Give the extent of all Plasmodium ovale-infected red blood cells.
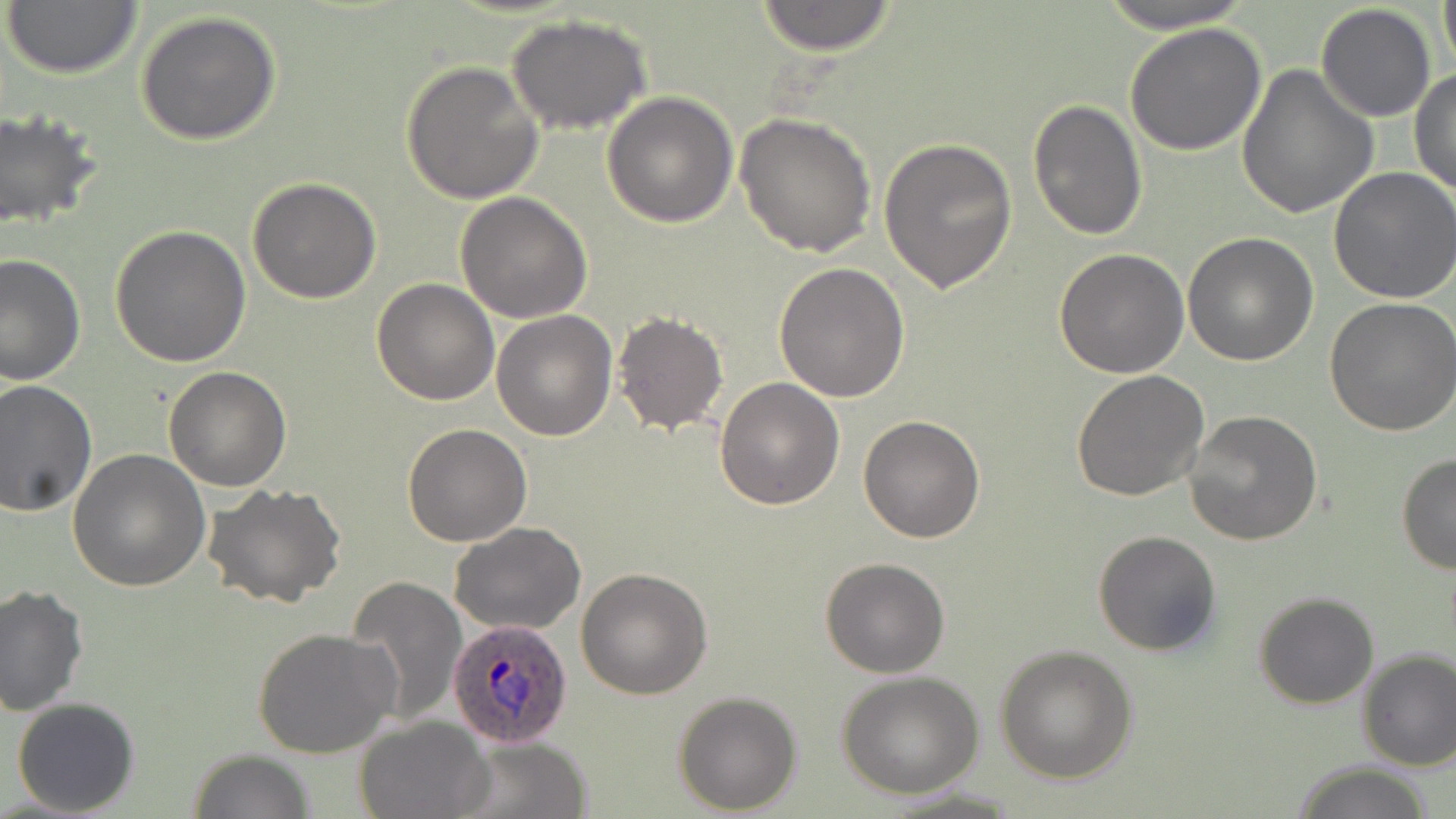

Approximate bounding boxes as (x1,y1)-(x2,y2) corner pairs in pixels.
Plasmodium ovale-infected red blood cells: (447,617)-(576,749).

Uninfected red blood cell locations: (752,0)-(900,54), (1091,0)-(1263,34), (1434,0)-(1456,75), (2,1)-(144,79), (1315,3)-(1437,121), (134,9)-(282,146), (506,15)-(655,135), (1124,22)-(1268,157), (400,60)-(544,205), (1238,65)-(1376,218), (1410,68)-(1455,197), (602,92)-(737,229), (1027,97)-(1148,240), (0,109)-(101,232), (732,112)-(878,256), (879,137)-(1020,295), (1328,167)-(1456,304), (247,176)-(382,303), (455,192)-(592,322), (110,225)-(251,367), (1182,231)-(1318,366), (1054,247)-(1189,377), (1,253)-(86,388), (773,261)-(910,402), (371,278)-(500,405), (1324,296)-(1456,436), (491,311)-(617,442), (612,311)-(729,437), (163,366)-(291,492), (1070,370)-(1209,503), (714,375)-(844,509), (0,380)-(97,516), (1184,409)-(1325,545), (857,414)-(986,542), (402,423)-(532,547), (67,449)-(210,593), (1395,453)-(1455,575), (203,483)-(348,607), (450,522)-(588,636), (1092,530)-(1221,657), (820,558)-(950,678), (575,567)-(713,699), (347,576)-(467,726), (0,584)-(90,719), (1253,592)-(1379,710), (253,627)-(399,760), (995,644)-(1138,783), (1356,648)-(1456,772), (835,670)-(985,798), (672,689)-(803,812), (11,696)-(141,817), (353,715)-(493,819), (452,736)-(594,819), (188,749)-(315,819), (1290,761)-(1438,819). Slide-level diagnosis: Plasmodium ovale. May-Grünwald-Giemsa-stained preparation. 1000x magnification. One field of a larger specimen. Thin blood film. Image is 1456×819 pixels. Optical microscopy.